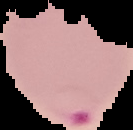

Summary:
  - Malaria status: parasitized
  - Preparation: thin blood film
  - Image type: segmented cell region on a black background
  - Image size: 133×130 pixels